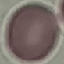
Summary:
  - Result: no malaria parasites detected
  - Capture: smartphone through the microscope eyepiece
  - Stain: Giemsa
  - Image type: automatically extracted cell patch, resized to 64 × 64 pixels
  - Preparation: thin blood film